Report the malaria status of this cell.
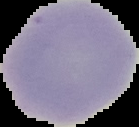
Uninfected.

Summary:
  - Preparation: thin blood film
  - Image size: 139×127 pixels
  - Image type: segmented cell region with the area outside set to black